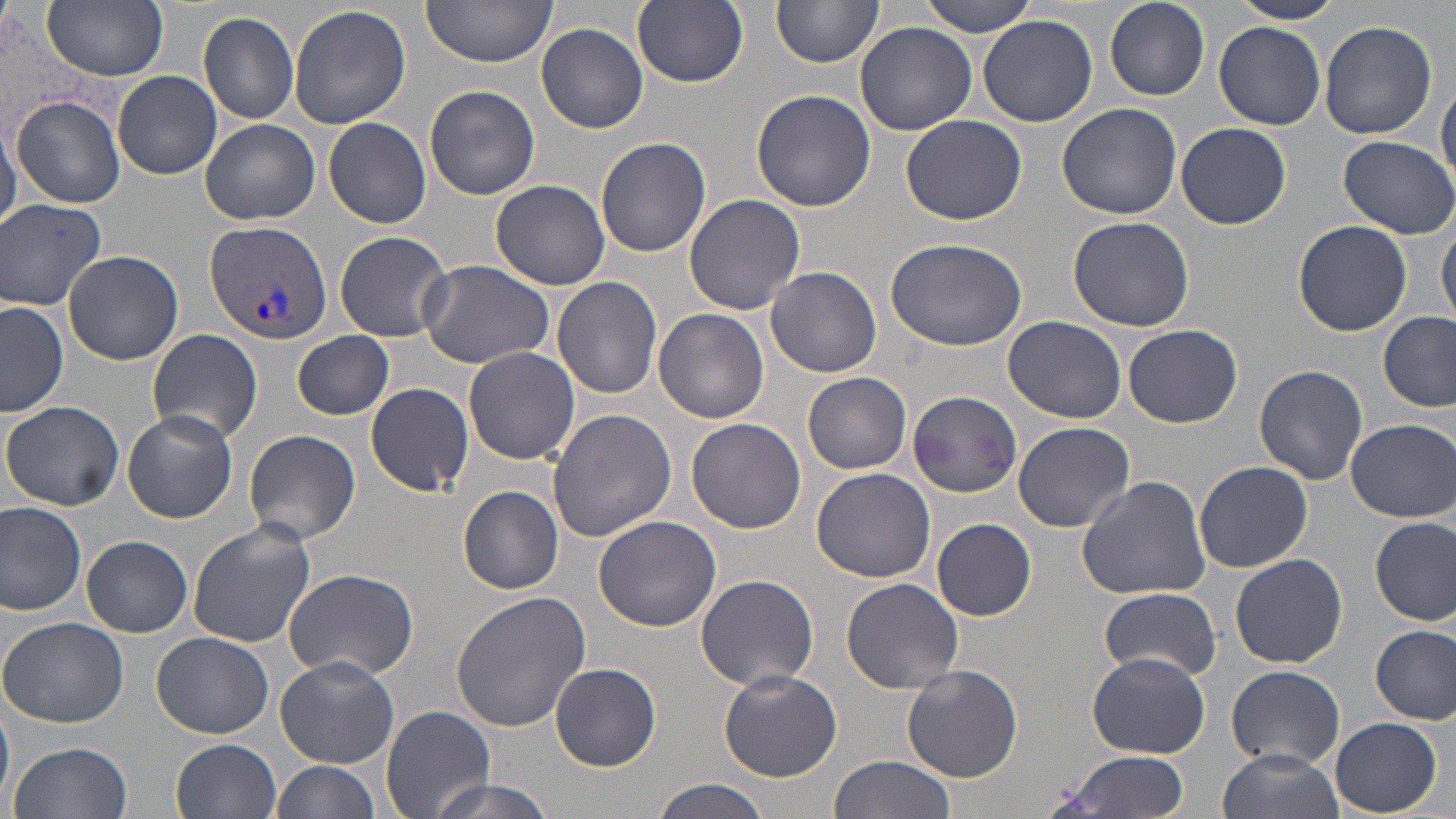 Approximate bounding boxes as (x1,y1)-(x2,y2) corner pairs in pixels. Uninfected red blood cell locations: (421,0)-(559,66), (631,0)-(749,89), (914,0)-(1043,36), (1230,0)-(1343,25), (43,1)-(170,80), (772,1)-(883,69), (1104,1)-(1209,100), (289,4)-(412,130), (197,11)-(300,125), (978,14)-(1098,127), (1317,20)-(1437,140), (854,22)-(977,134), (1213,22)-(1325,129), (536,23)-(648,133), (113,70)-(222,179), (1436,79)-(1456,189), (424,85)-(540,200), (749,87)-(876,213), (10,96)-(126,207), (1057,102)-(1183,219), (901,113)-(1027,226), (322,116)-(431,228), (0,117)-(20,240), (200,119)-(319,224), (1176,122)-(1291,229), (596,136)-(712,258), (1338,136)-(1456,238), (489,178)-(611,291), (683,194)-(806,317), (0,197)-(109,312), (1067,216)-(1195,332), (1438,218)-(1456,324), (1293,219)-(1412,337), (335,231)-(452,341), (884,237)-(1028,351), (62,248)-(184,366), (416,258)-(555,368), (766,266)-(882,378), (552,276)-(663,398), (0,301)-(70,418), (654,309)-(770,424), (1377,311)-(1454,413), (1002,314)-(1128,423), (1123,324)-(1241,428), (148,329)-(263,443), (292,332)-(394,419), (463,346)-(580,464), (1255,363)-(1369,485), (803,372)-(912,474), (365,381)-(475,496), (907,388)-(1026,497), (2,400)-(125,511), (547,408)-(676,541), (123,410)-(237,523), (1345,417)-(1455,523), (686,418)-(808,534), (1012,420)-(1136,531), (242,428)-(361,545), (1193,462)-(1313,572), (810,467)-(935,583), (1076,476)-(1211,601), (459,487)-(564,595), (0,503)-(86,616), (593,515)-(722,633), (1371,515)-(1455,626), (932,517)-(1037,621), (186,521)-(316,648), (81,536)-(193,637), (1229,553)-(1347,669), (282,569)-(419,681), (694,573)-(820,691), (842,577)-(963,693), (1099,587)-(1221,681), (450,590)-(590,731), (1,616)-(129,728), (1371,623)-(1454,724), (152,631)-(273,739), (1088,651)-(1209,758), (275,655)-(400,767), (551,662)-(661,771), (902,665)-(1023,782), (1227,665)-(1348,768), (716,668)-(841,783), (0,694)-(15,810), (381,705)-(495,819), (1329,715)-(1443,817), (171,738)-(281,819), (8,741)-(134,819), (1217,749)-(1344,819), (1055,751)-(1193,819), (828,755)-(956,819), (272,760)-(382,819), (420,776)-(558,819), (649,778)-(774,819). Plasmodium vivax-infected red blood cell locations: (204,219)-(332,346). Slide-level diagnosis: Plasmodium vivax. One field of a larger specimen. Light microscopy. May-Grünwald-Giemsa stain. Thin blood smear. 1000x magnification. Image is 1456×819 pixels.